Report the malaria status of this cell.
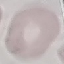
It is uninfected.

Thin smear of blood. Acquired by smartphone through the microscope eyepiece. Automatically extracted cell patch, resized to 64 × 64 pixels. Giemsa-stained preparation.